State which cell type is depicted.
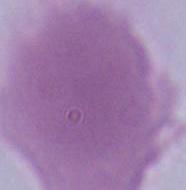

An erythrocyte.

Captured at 1000x magnification. Photomicrograph.